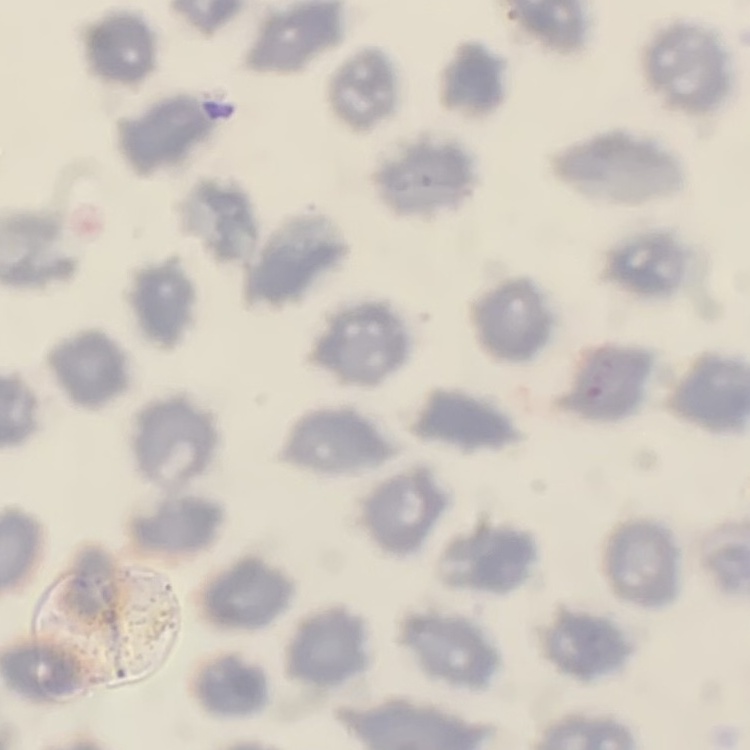

{
  "erythrocyte_morphology": "no rouleaux formation",
  "stain": "Field's or Giemsa",
  "image_type": "square crop of a larger photomicrograph",
  "preparation": "thin blood smear"
}